Describe the morphology of the erythrocytes.
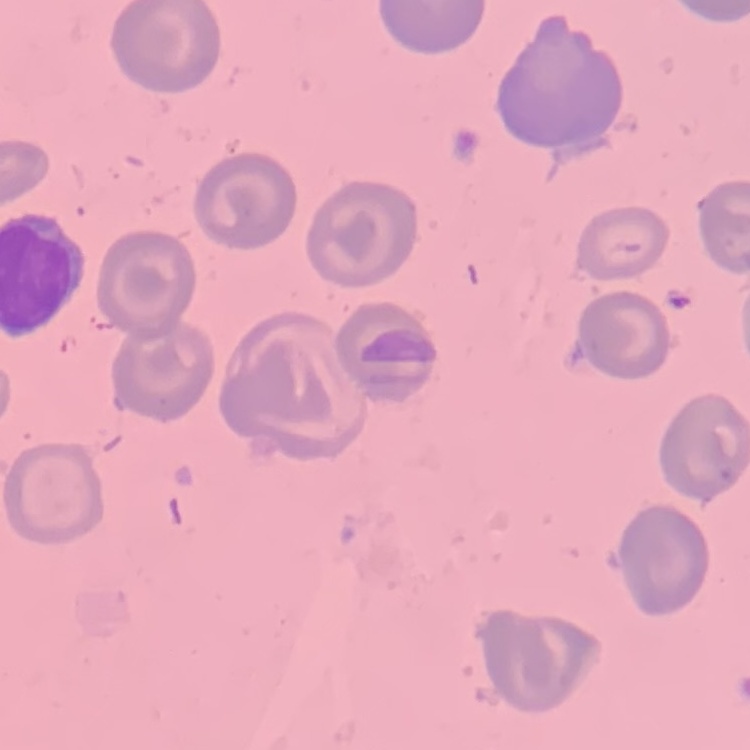
They show no rouleaux formation.

Square crop of a larger photomicrograph. Thin blood film. Field's or Giemsa stain.